Name the blood parasite species.
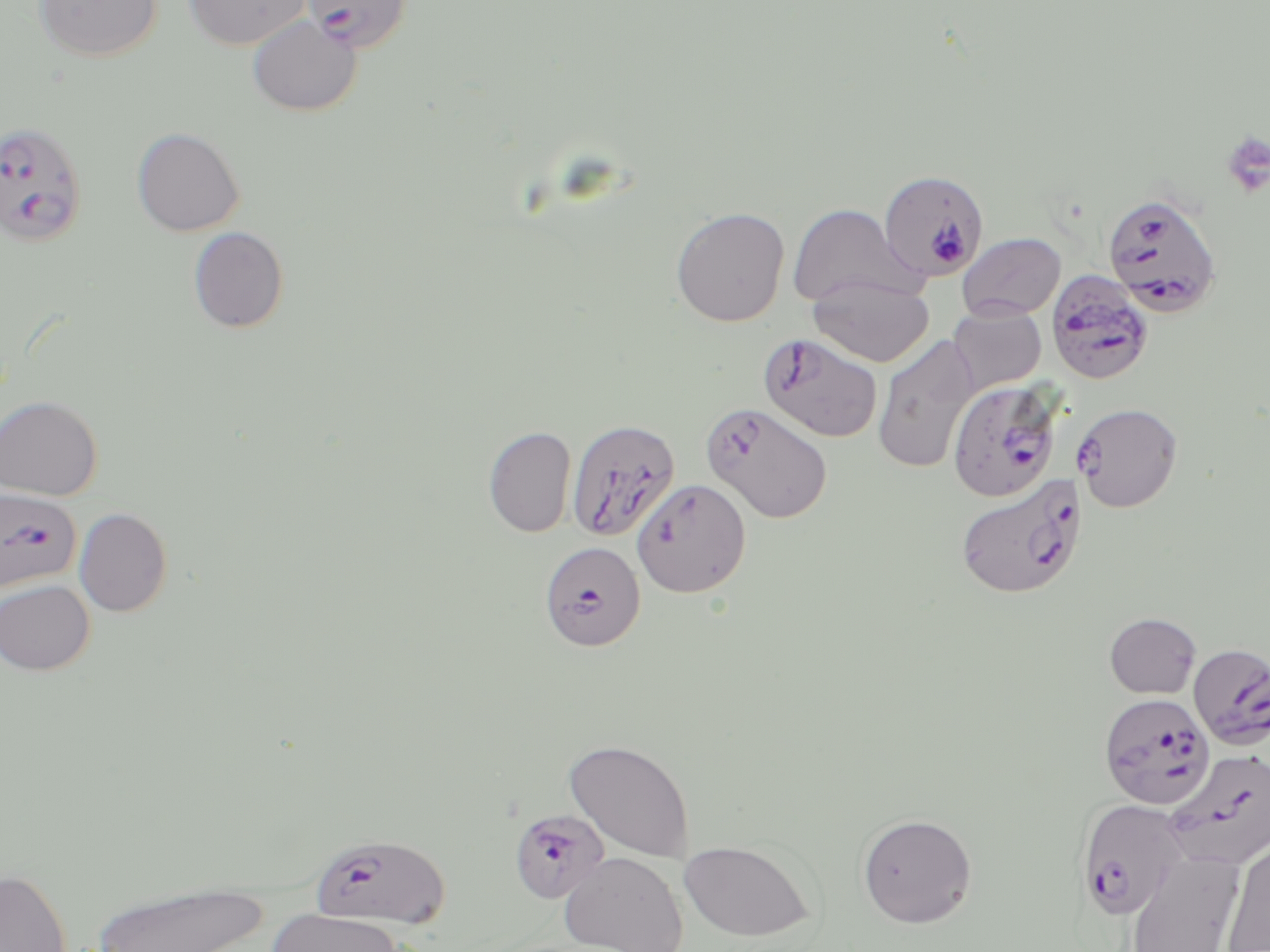
Plasmodium falciparum.

modality = light microscopy
image size = 1270×952 pixels
Plasmodium falciparum-infected red blood cell locations = approximate bounding boxes as named x1/y1/x2/y2 corners in pixels: (x1=303, y1=0, x2=413, y2=53), (x1=0, y1=121, x2=89, y2=248), (x1=879, y1=169, x2=991, y2=283), (x1=1102, y1=191, x2=1223, y2=317), (x1=1046, y1=269, x2=1155, y2=386), (x1=757, y1=333, x2=882, y2=443), (x1=947, y1=379, x2=1063, y2=502), (x1=1073, y1=402, x2=1183, y2=512), (x1=701, y1=403, x2=833, y2=523), (x1=566, y1=418, x2=680, y2=543), (x1=955, y1=473, x2=1086, y2=599), (x1=632, y1=478, x2=751, y2=598), (x1=0, y1=488, x2=83, y2=593), (x1=539, y1=541, x2=645, y2=651), (x1=1188, y1=642, x2=1270, y2=748), (x1=1098, y1=693, x2=1215, y2=809), (x1=1165, y1=749, x2=1270, y2=869), (x1=1076, y1=798, x2=1190, y2=920), (x1=508, y1=808, x2=610, y2=904), (x1=309, y1=833, x2=449, y2=928)
magnification = 1000x
preparation = thin blood smear
platelet locations = approximate bounding boxes as named x1/y1/x2/y2 corners in pixels: (x1=1220, y1=131, x2=1270, y2=198)
field of view = single
stain = May-Grünwald-Giemsa
uninfected red blood cell locations = approximate bounding boxes as named x1/y1/x2/y2 corners in pixels: (x1=34, y1=0, x2=162, y2=61), (x1=184, y1=0, x2=310, y2=50), (x1=247, y1=15, x2=361, y2=116), (x1=132, y1=127, x2=244, y2=236), (x1=788, y1=203, x2=916, y2=308), (x1=670, y1=207, x2=790, y2=327), (x1=188, y1=226, x2=289, y2=334), (x1=957, y1=232, x2=1066, y2=320), (x1=809, y1=275, x2=934, y2=367), (x1=948, y1=304, x2=1046, y2=394), (x1=871, y1=334, x2=978, y2=475), (x1=0, y1=395, x2=103, y2=500), (x1=483, y1=425, x2=577, y2=537), (x1=74, y1=507, x2=173, y2=617), (x1=0, y1=579, x2=95, y2=675), (x1=1104, y1=612, x2=1202, y2=698), (x1=564, y1=738, x2=695, y2=862), (x1=856, y1=813, x2=977, y2=927), (x1=1220, y1=838, x2=1270, y2=951), (x1=678, y1=839, x2=815, y2=942), (x1=559, y1=851, x2=688, y2=952), (x1=1123, y1=851, x2=1244, y2=952), (x1=0, y1=868, x2=71, y2=952), (x1=88, y1=879, x2=270, y2=952), (x1=266, y1=907, x2=405, y2=952)